Report the malaria status of this cell.
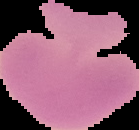
It is uninfected.

Image is 139×130 pixels. The area outside the segmented cell region is set to black. From a thin blood smear.